Identify the cell.
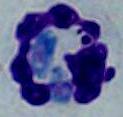
A leukocyte.

{
  "modality": "micrograph",
  "magnification": "1000x"
}